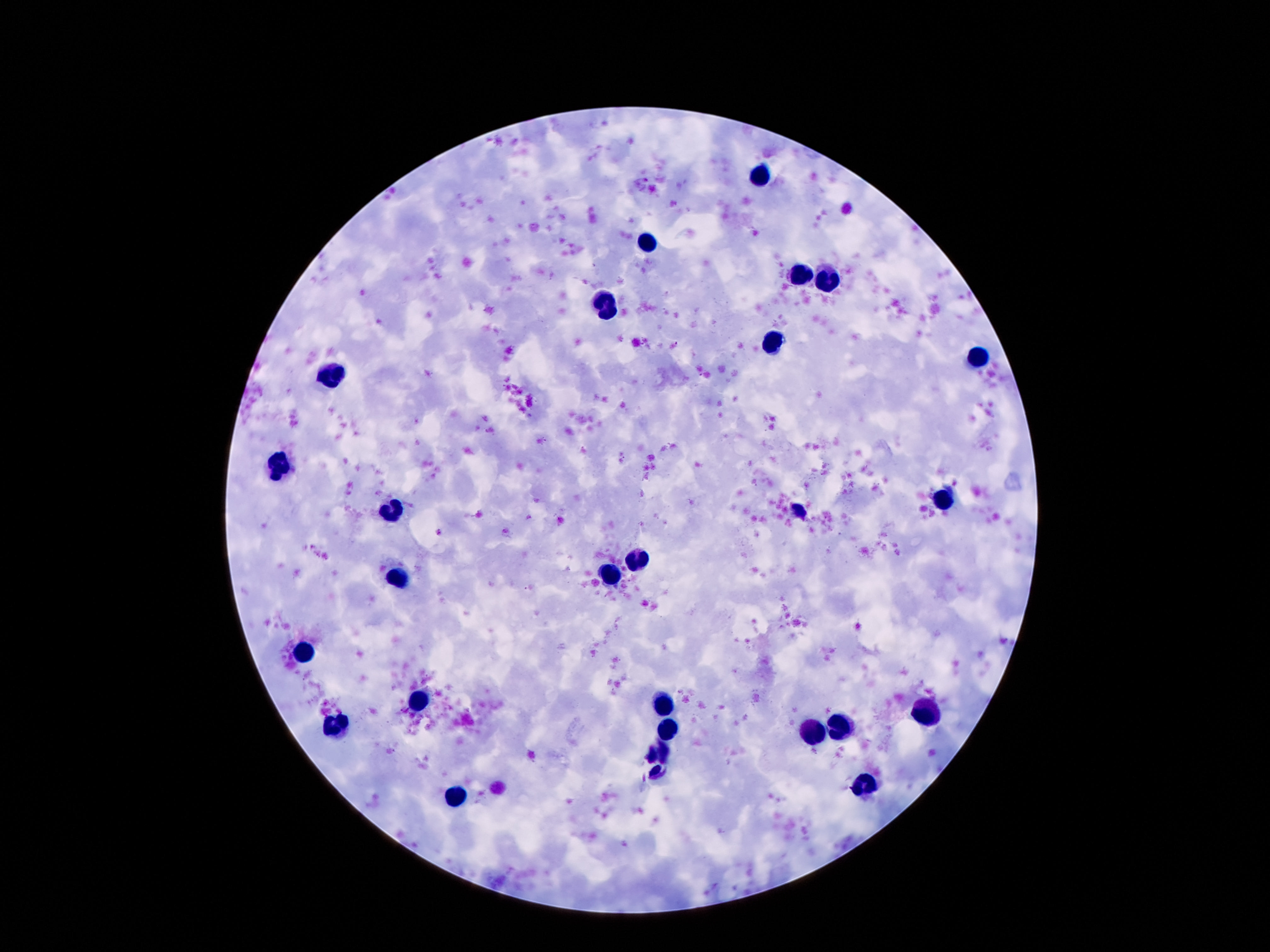
Approximate centers as [x, y] in pixels.
Summary:
  - Leukocyte locations: [761, 175], [649, 245], [800, 270], [823, 280], [607, 307], [775, 343], [975, 357], [331, 375], [282, 465], [941, 500], [392, 511], [800, 513], [633, 558], [612, 576], [398, 580], [304, 647], [422, 702], [662, 704], [924, 713], [840, 724], [336, 726], [669, 731], [812, 736], [657, 752], [867, 786], [455, 798]
  - Image size: 1270×952 pixels
  - Preparation: thick blood film
  - Stain: Giemsa
  - Magnification: 100x
  - Capture: smartphone camera through the microscope eyepiece
  - Field of view: single
  - Patient malaria status: negative